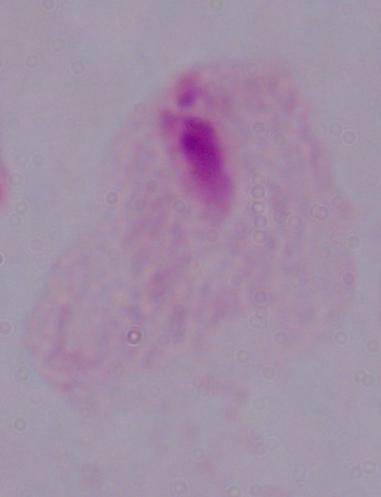

{
  "identification": "trichomonad",
  "modality": "micrograph",
  "magnification": "1000x"
}